Classify this cell by malaria status.
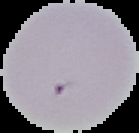

Uninfected.

preparation = thin blood film
image size = 139×133 pixels
image type = cell region segmented out of the field of view; surrounding area masked to black